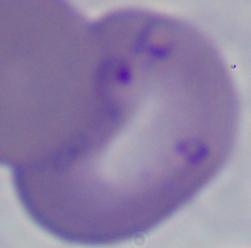
Summary:
  - Identification: Babesia
  - Modality: micrograph
  - Magnification: 1000x